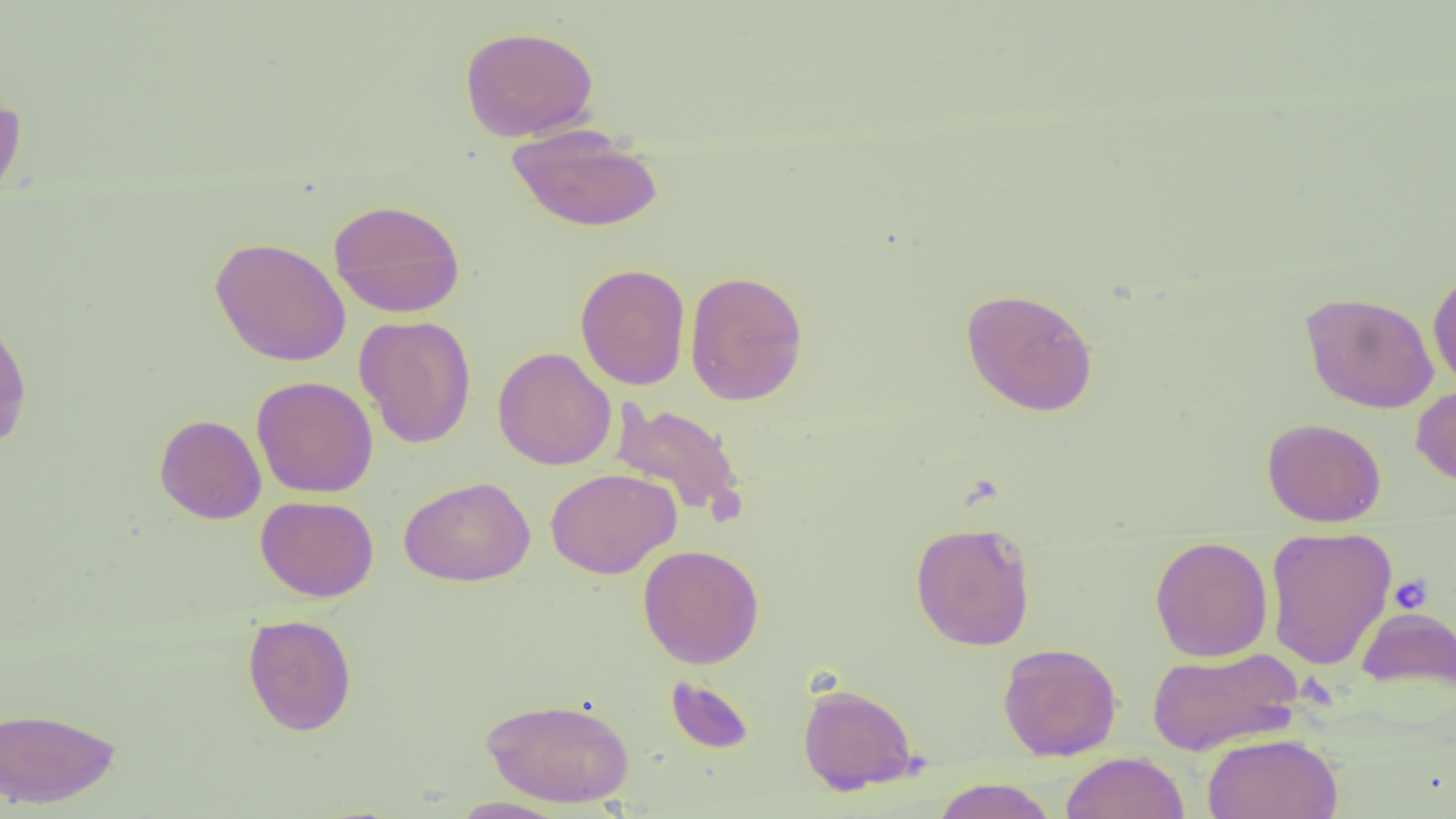

slide-level diagnosis = negative for blood parasites
uninfected red blood cell locations = approximate bounding boxes as (x1,y1)-(x2,y2) corner pairs in pixels: (459,25)-(599,141), (0,82)-(28,204), (506,126)-(664,232), (328,199)-(466,318), (210,236)-(350,366), (575,263)-(690,390), (1427,268)-(1456,391), (684,269)-(809,405), (960,287)-(1099,416), (1300,291)-(1439,414), (0,313)-(33,451), (354,315)-(476,448), (493,347)-(616,470), (251,376)-(378,498), (1411,384)-(1456,490), (609,400)-(746,522), (154,413)-(266,524), (1261,417)-(1387,527), (545,468)-(681,579), (399,476)-(536,587), (256,495)-(379,601), (910,520)-(1036,651), (1265,525)-(1397,669), (1150,535)-(1273,662), (638,544)-(764,668), (1356,606)-(1456,695), (242,613)-(357,736), (997,643)-(1122,761), (1146,646)-(1302,756), (664,675)-(755,754), (797,683)-(919,795), (481,696)-(635,807), (0,705)-(121,809), (1202,732)-(1343,819), (1061,751)-(1189,819), (931,777)-(1058,819), (450,797)-(570,818)
field of view = one of a larger specimen
platelet locations = approximate bounding boxes as (x1,y1)-(x2,y2) corner pairs in pixels: (1388,574)-(1434,614)
image size = 1456×819 pixels
preparation = thin blood film
modality = light microscopy
magnification = 1000x